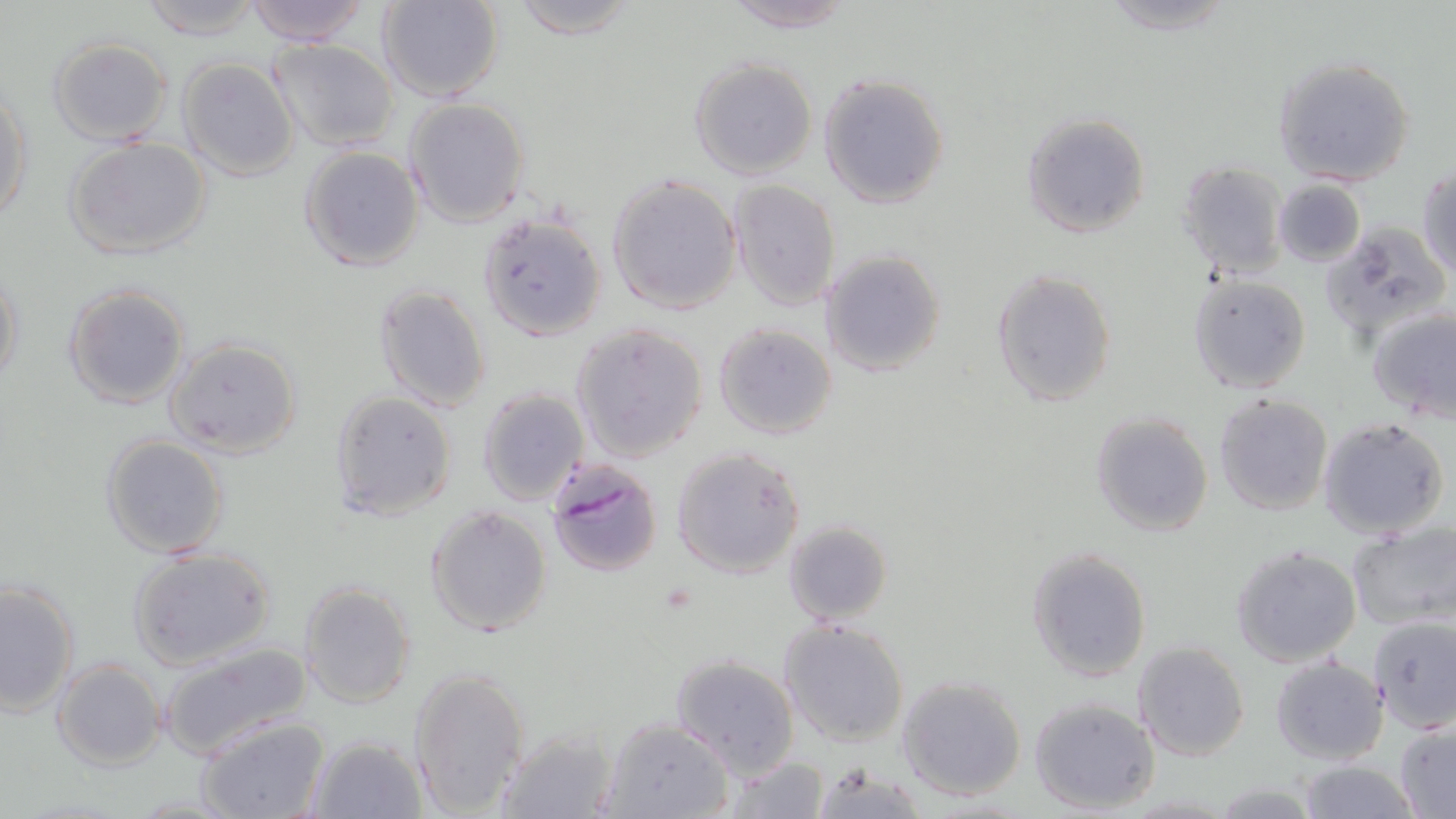 Approximate bounding boxes as named x1/y1/x2/y2 corners in pixels. Plasmodium falciparum-infected red blood cell locations: (x1=545, y1=458, x2=665, y2=579). Uninfected red blood cell locations: (x1=134, y1=0, x2=269, y2=40), (x1=241, y1=0, x2=374, y2=45), (x1=378, y1=0, x2=503, y2=103), (x1=503, y1=0, x2=642, y2=38), (x1=720, y1=0, x2=859, y2=31), (x1=1098, y1=0, x2=1238, y2=34), (x1=47, y1=36, x2=175, y2=146), (x1=267, y1=37, x2=400, y2=152), (x1=177, y1=56, x2=299, y2=181), (x1=1272, y1=56, x2=1416, y2=187), (x1=688, y1=58, x2=818, y2=179), (x1=818, y1=73, x2=950, y2=209), (x1=0, y1=86, x2=32, y2=227), (x1=405, y1=98, x2=529, y2=227), (x1=1019, y1=113, x2=1151, y2=239), (x1=63, y1=136, x2=211, y2=261), (x1=299, y1=146, x2=425, y2=272), (x1=1176, y1=160, x2=1289, y2=279), (x1=1417, y1=164, x2=1456, y2=277), (x1=607, y1=174, x2=742, y2=315), (x1=728, y1=179, x2=841, y2=311), (x1=1273, y1=180, x2=1365, y2=267), (x1=477, y1=209, x2=608, y2=340), (x1=1320, y1=220, x2=1451, y2=343), (x1=819, y1=249, x2=947, y2=378), (x1=1, y1=258, x2=24, y2=393), (x1=992, y1=269, x2=1118, y2=409), (x1=1188, y1=273, x2=1310, y2=394), (x1=63, y1=283, x2=191, y2=410), (x1=372, y1=283, x2=492, y2=412), (x1=1367, y1=305, x2=1456, y2=422), (x1=572, y1=322, x2=707, y2=462), (x1=713, y1=322, x2=838, y2=440), (x1=166, y1=339, x2=302, y2=459), (x1=476, y1=387, x2=589, y2=508), (x1=328, y1=390, x2=458, y2=520), (x1=1213, y1=393, x2=1333, y2=517), (x1=1089, y1=412, x2=1214, y2=537), (x1=1318, y1=416, x2=1449, y2=539), (x1=99, y1=434, x2=229, y2=559), (x1=671, y1=445, x2=806, y2=579), (x1=425, y1=504, x2=553, y2=638), (x1=782, y1=519, x2=892, y2=626), (x1=1347, y1=523, x2=1455, y2=630), (x1=1230, y1=545, x2=1363, y2=667), (x1=1024, y1=546, x2=1153, y2=683), (x1=128, y1=547, x2=277, y2=669), (x1=0, y1=577, x2=79, y2=716), (x1=297, y1=581, x2=417, y2=709), (x1=1368, y1=615, x2=1456, y2=734), (x1=778, y1=619, x2=910, y2=749), (x1=157, y1=640, x2=311, y2=759), (x1=1133, y1=641, x2=1251, y2=762), (x1=670, y1=653, x2=798, y2=778), (x1=1270, y1=657, x2=1390, y2=765), (x1=52, y1=660, x2=164, y2=770), (x1=409, y1=667, x2=531, y2=817), (x1=897, y1=674, x2=1026, y2=800), (x1=1029, y1=697, x2=1160, y2=815), (x1=197, y1=714, x2=332, y2=819), (x1=601, y1=717, x2=734, y2=819), (x1=1394, y1=720, x2=1456, y2=817), (x1=494, y1=726, x2=620, y2=819), (x1=305, y1=733, x2=428, y2=819), (x1=724, y1=757, x2=828, y2=819), (x1=1296, y1=760, x2=1420, y2=818), (x1=808, y1=763, x2=932, y2=817), (x1=1208, y1=780, x2=1323, y2=817). Slide-level diagnosis: Plasmodium falciparum. Thin blood film. Captured at 1000x magnification. One field of a larger specimen. May-Grünwald-Giemsa-stained preparation. Image is 1456×819 pixels. Optical microscopy.